Assess this cell for malaria.
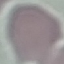
Uninfected.

Giemsa-stained preparation. Cell patch, automatically extracted from a larger field of view and resized to 64 × 64 pixels. Thin blood film. Photographed with a smartphone camera at the microscope eyepiece.